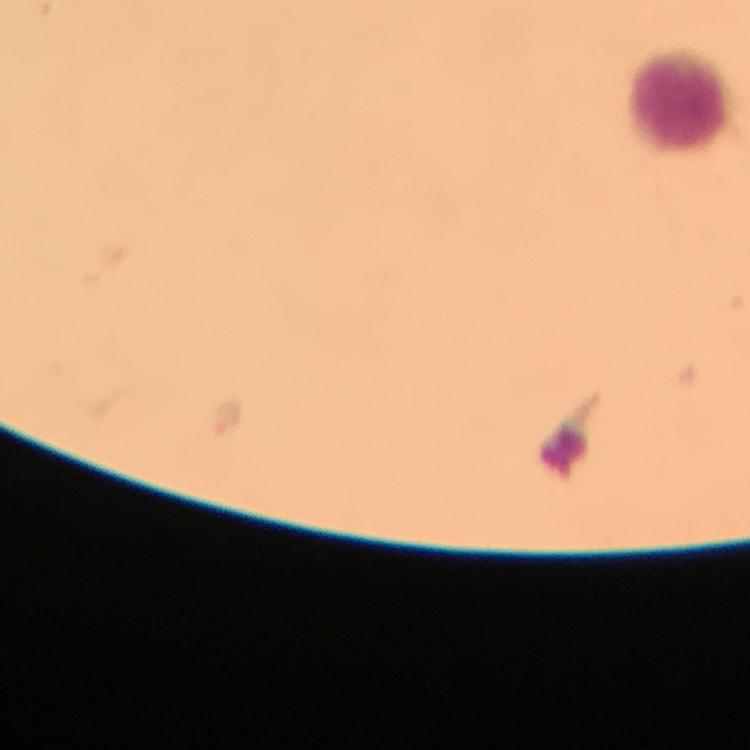
Approximate object centers, in pixels from the top-left corner.
Summary:
  - Plasmodium parasite locations: (x=226, y=416)
  - Leukocyte locations: (x=681, y=98)
  - Magnification: 100x
  - Image size: 750×750 pixels
  - Stain: Giemsa
  - Immersion oil: applied
  - Context: from a malaria diagnostic workup
  - Preparation: thick smear
  - Cropped from: one field of view
  - Capture: smartphone camera through the microscope